Comment on the morphology of the erythrocytes.
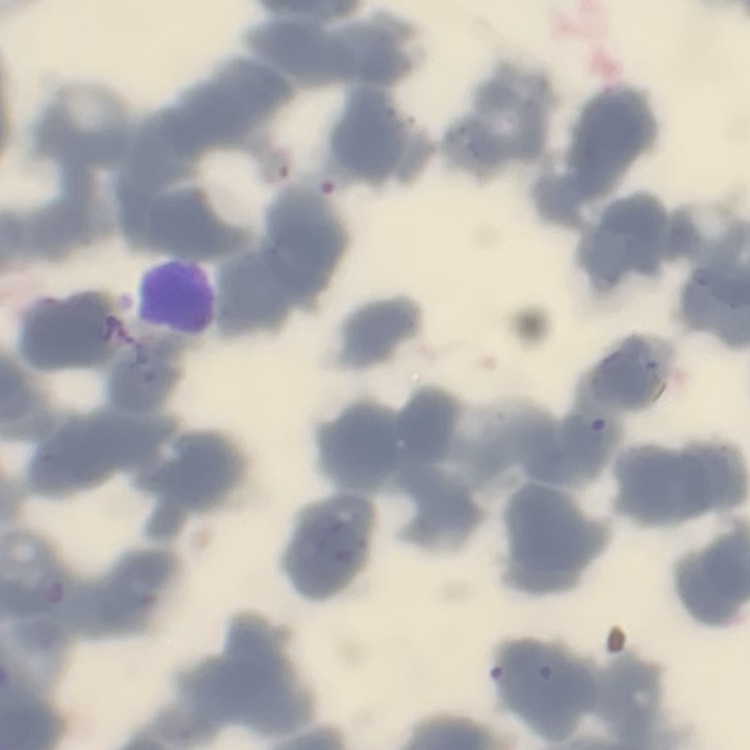

Rouleaux formation.

Thin blood film. Field's or Giemsa stain. Square crop of a larger photomicrograph.